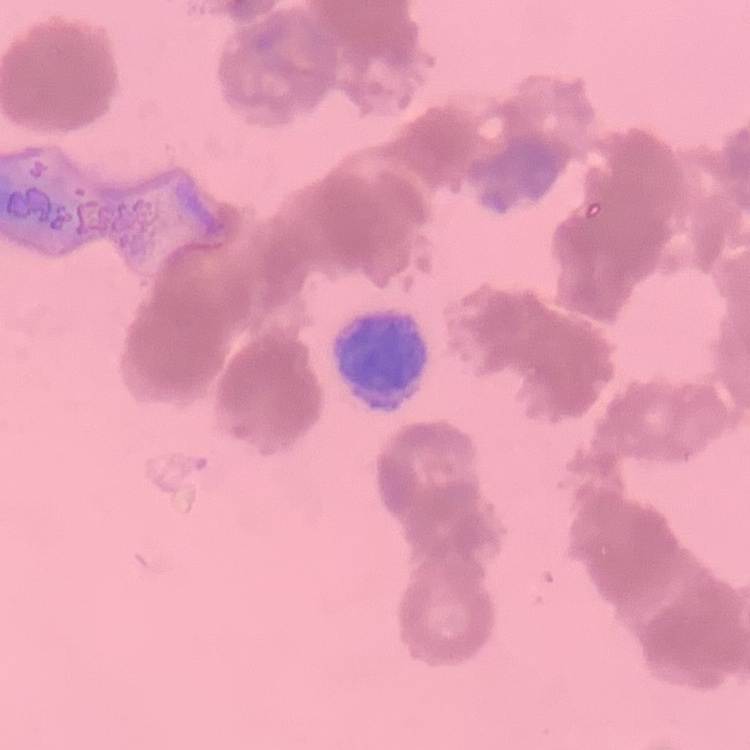
red blood cell morphology = rouleaux formation
preparation = thin peripheral smear
stain = Field's or Giemsa
image type = square crop of a larger photomicrograph